State the blood parasite species.
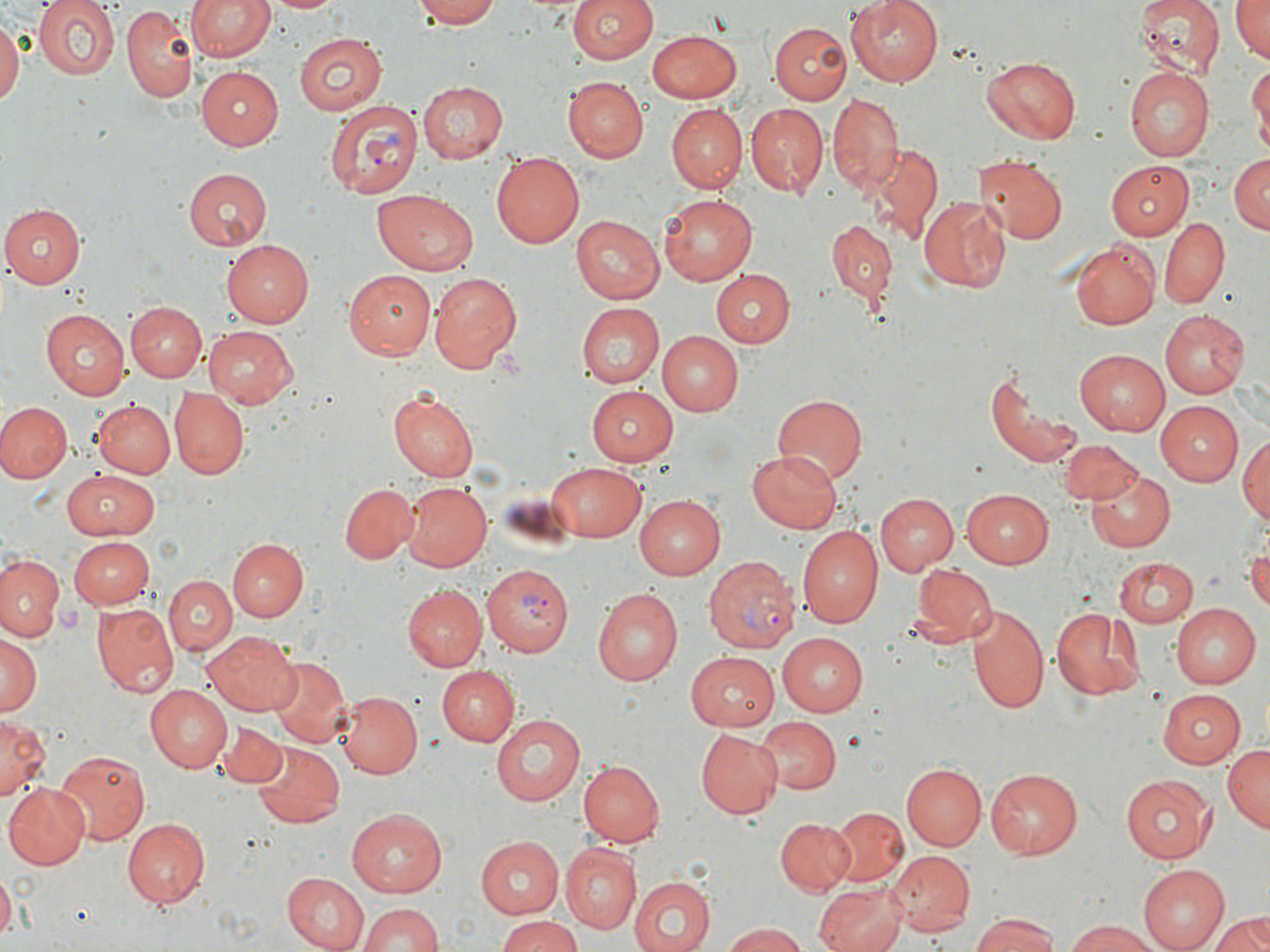

Plasmodium vivax.

Approximate bounding boxes as named x1/y1/x2/y2 corners in pixels. Uninfected red blood cell locations: (x1=34, y1=0, x2=119, y2=81), (x1=187, y1=0, x2=274, y2=62), (x1=267, y1=0, x2=344, y2=15), (x1=410, y1=0, x2=503, y2=28), (x1=568, y1=0, x2=658, y2=64), (x1=846, y1=0, x2=944, y2=86), (x1=1134, y1=0, x2=1226, y2=77), (x1=1229, y1=0, x2=1269, y2=62), (x1=122, y1=6, x2=199, y2=101), (x1=0, y1=16, x2=22, y2=108), (x1=769, y1=23, x2=851, y2=103), (x1=647, y1=31, x2=744, y2=102), (x1=294, y1=33, x2=385, y2=116), (x1=983, y1=56, x2=1082, y2=144), (x1=1248, y1=61, x2=1270, y2=154), (x1=197, y1=67, x2=284, y2=149), (x1=1124, y1=68, x2=1213, y2=162), (x1=564, y1=78, x2=647, y2=161), (x1=419, y1=82, x2=509, y2=163), (x1=827, y1=92, x2=904, y2=196), (x1=745, y1=104, x2=827, y2=197), (x1=666, y1=105, x2=746, y2=193), (x1=869, y1=142, x2=944, y2=243), (x1=492, y1=153, x2=587, y2=247), (x1=975, y1=155, x2=1066, y2=247), (x1=1227, y1=155, x2=1269, y2=234), (x1=1108, y1=161, x2=1191, y2=240), (x1=182, y1=169, x2=271, y2=249), (x1=373, y1=189, x2=478, y2=274), (x1=658, y1=193, x2=757, y2=283), (x1=918, y1=195, x2=1009, y2=291), (x1=3, y1=204, x2=85, y2=287), (x1=572, y1=215, x2=664, y2=304), (x1=1160, y1=218, x2=1228, y2=308), (x1=828, y1=221, x2=895, y2=303), (x1=1071, y1=240, x2=1160, y2=330), (x1=222, y1=241, x2=314, y2=327), (x1=345, y1=270, x2=433, y2=358), (x1=710, y1=270, x2=795, y2=345), (x1=429, y1=273, x2=522, y2=372), (x1=125, y1=302, x2=206, y2=381), (x1=576, y1=304, x2=664, y2=389), (x1=1160, y1=309, x2=1254, y2=399), (x1=41, y1=310, x2=129, y2=399), (x1=202, y1=325, x2=299, y2=406), (x1=659, y1=331, x2=744, y2=415), (x1=1074, y1=350, x2=1169, y2=434), (x1=984, y1=368, x2=1080, y2=470), (x1=586, y1=387, x2=679, y2=465), (x1=171, y1=388, x2=249, y2=479), (x1=389, y1=389, x2=479, y2=482), (x1=771, y1=394, x2=867, y2=483), (x1=91, y1=398, x2=175, y2=479), (x1=0, y1=401, x2=71, y2=484), (x1=1154, y1=401, x2=1243, y2=483), (x1=1237, y1=431, x2=1270, y2=530), (x1=1059, y1=439, x2=1142, y2=505), (x1=747, y1=450, x2=844, y2=533), (x1=545, y1=461, x2=646, y2=540), (x1=66, y1=468, x2=158, y2=539), (x1=1088, y1=469, x2=1175, y2=553), (x1=341, y1=483, x2=418, y2=563), (x1=400, y1=483, x2=492, y2=571), (x1=962, y1=488, x2=1056, y2=565), (x1=875, y1=492, x2=958, y2=576), (x1=633, y1=495, x2=722, y2=579), (x1=797, y1=526, x2=884, y2=629), (x1=69, y1=536, x2=154, y2=610), (x1=226, y1=538, x2=306, y2=622), (x1=1247, y1=543, x2=1270, y2=614), (x1=0, y1=552, x2=64, y2=641), (x1=1113, y1=557, x2=1196, y2=627), (x1=907, y1=561, x2=995, y2=651), (x1=700, y1=569, x2=789, y2=727), (x1=163, y1=574, x2=237, y2=654), (x1=405, y1=585, x2=488, y2=671), (x1=592, y1=588, x2=683, y2=686), (x1=92, y1=602, x2=178, y2=695), (x1=1169, y1=603, x2=1259, y2=688), (x1=967, y1=605, x2=1050, y2=719), (x1=1048, y1=606, x2=1146, y2=698), (x1=202, y1=631, x2=301, y2=715), (x1=775, y1=632, x2=868, y2=718), (x1=0, y1=636, x2=40, y2=719), (x1=684, y1=651, x2=779, y2=730), (x1=266, y1=656, x2=351, y2=750), (x1=439, y1=665, x2=520, y2=743), (x1=143, y1=687, x2=230, y2=773), (x1=1155, y1=688, x2=1247, y2=766), (x1=338, y1=690, x2=422, y2=777), (x1=490, y1=713, x2=591, y2=806), (x1=755, y1=716, x2=839, y2=795), (x1=0, y1=717, x2=48, y2=803), (x1=215, y1=720, x2=285, y2=788), (x1=695, y1=729, x2=782, y2=818), (x1=250, y1=742, x2=344, y2=827), (x1=1223, y1=746, x2=1269, y2=831), (x1=52, y1=748, x2=150, y2=845), (x1=580, y1=760, x2=664, y2=846), (x1=901, y1=762, x2=986, y2=849), (x1=986, y1=768, x2=1085, y2=859), (x1=1121, y1=775, x2=1215, y2=863), (x1=4, y1=784, x2=88, y2=870), (x1=827, y1=806, x2=908, y2=888), (x1=348, y1=808, x2=448, y2=896), (x1=775, y1=817, x2=856, y2=895), (x1=121, y1=818, x2=210, y2=907), (x1=474, y1=836, x2=565, y2=917), (x1=562, y1=844, x2=642, y2=933), (x1=887, y1=850, x2=974, y2=933), (x1=1138, y1=865, x2=1231, y2=952), (x1=0, y1=871, x2=15, y2=937), (x1=281, y1=873, x2=369, y2=951), (x1=629, y1=877, x2=717, y2=952), (x1=813, y1=883, x2=908, y2=952), (x1=357, y1=904, x2=445, y2=952), (x1=1211, y1=909, x2=1270, y2=952), (x1=969, y1=912, x2=1061, y2=952), (x1=494, y1=915, x2=580, y2=952), (x1=1063, y1=919, x2=1167, y2=952), (x1=719, y1=922, x2=808, y2=952). Plasmodium vivax-infected red blood cell locations: (x1=323, y1=98, x2=421, y2=201), (x1=705, y1=555, x2=798, y2=653), (x1=486, y1=563, x2=573, y2=656). Platelet locations: (x1=56, y1=601, x2=84, y2=635). Captured at 1000x magnification. Thin blood smear. Optical microscopy. Single field of view. Image is 1270×952 pixels. May-Grünwald-Giemsa-stained preparation.